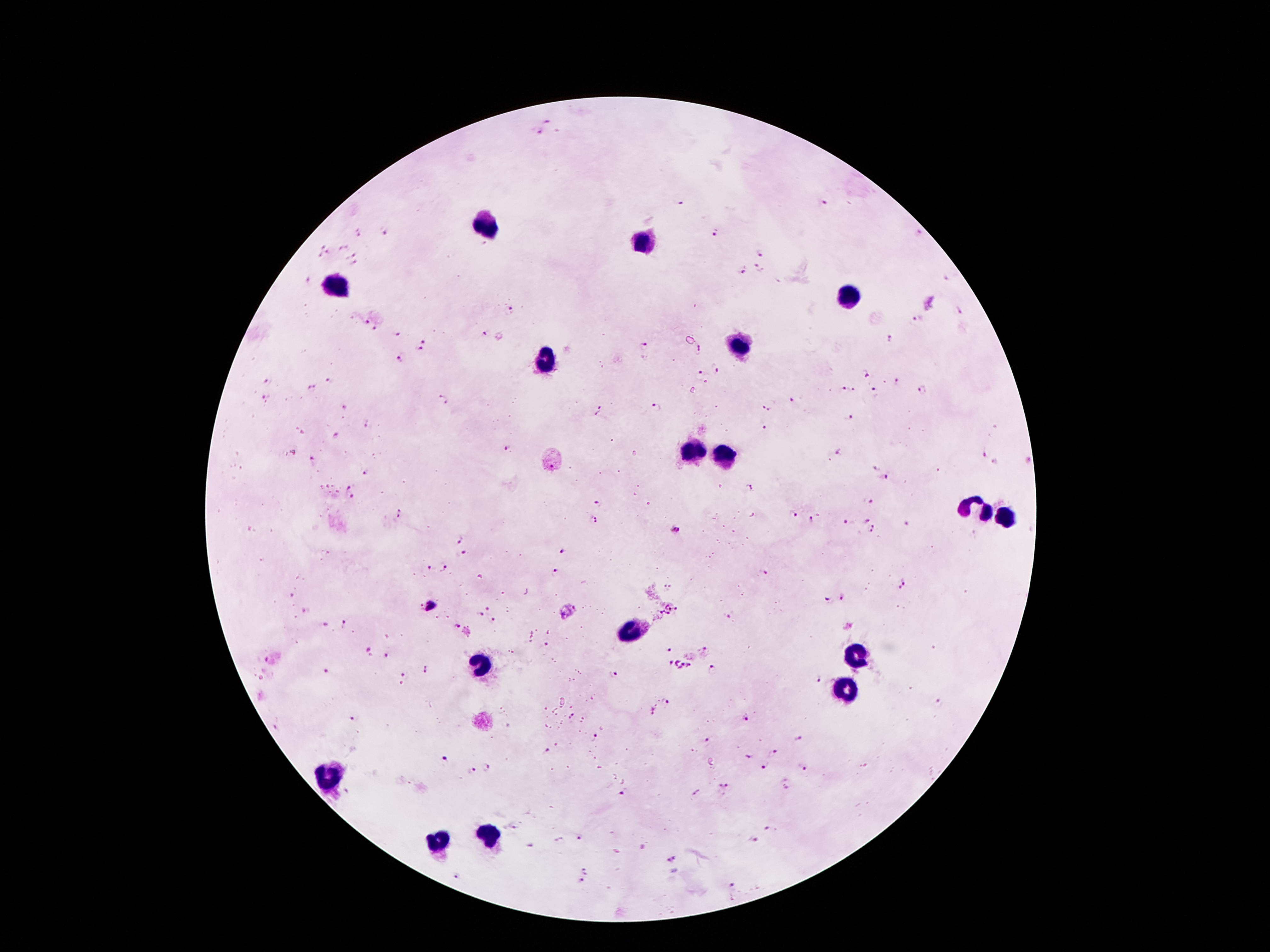

Approximate object centers, in pixels from the top-left corner.
Summary:
  - Plasmodium parasite locations: (x=548, y=121), (x=536, y=131), (x=680, y=202), (x=824, y=202), (x=358, y=231), (x=716, y=231), (x=383, y=233), (x=919, y=234), (x=323, y=244), (x=342, y=247), (x=330, y=252), (x=761, y=252), (x=351, y=254), (x=318, y=255), (x=354, y=262), (x=743, y=269), (x=760, y=269), (x=309, y=278), (x=945, y=279), (x=931, y=303), (x=511, y=310), (x=959, y=311), (x=918, y=320), (x=365, y=321), (x=374, y=328), (x=485, y=335), (x=398, y=336), (x=887, y=340), (x=423, y=341), (x=644, y=346), (x=420, y=348), (x=699, y=349), (x=399, y=360), (x=716, y=368), (x=700, y=374), (x=867, y=374), (x=328, y=381), (x=267, y=382), (x=897, y=383), (x=311, y=389), (x=854, y=390), (x=923, y=390), (x=844, y=391), (x=875, y=393), (x=267, y=398), (x=443, y=398), (x=791, y=400), (x=344, y=406), (x=601, y=406), (x=657, y=408), (x=767, y=408), (x=596, y=414), (x=849, y=416), (x=366, y=425), (x=763, y=428), (x=336, y=434), (x=840, y=449), (x=507, y=450), (x=984, y=453), (x=313, y=459), (x=1026, y=460), (x=995, y=461), (x=875, y=467), (x=366, y=470), (x=885, y=478), (x=350, y=487), (x=748, y=487), (x=352, y=495), (x=598, y=500), (x=868, y=500), (x=792, y=514), (x=400, y=515), (x=594, y=518), (x=866, y=518), (x=812, y=519), (x=847, y=522), (x=907, y=524), (x=872, y=529), (x=675, y=530), (x=460, y=538), (x=464, y=551), (x=562, y=552), (x=428, y=566), (x=442, y=566), (x=556, y=571), (x=763, y=572), (x=903, y=583), (x=668, y=587), (x=293, y=595), (x=843, y=596), (x=827, y=599), (x=431, y=606), (x=488, y=608), (x=669, y=610), (x=304, y=611), (x=479, y=614), (x=729, y=616), (x=495, y=620), (x=342, y=624), (x=325, y=626), (x=458, y=626), (x=548, y=646), (x=705, y=647), (x=670, y=648), (x=368, y=650), (x=386, y=656), (x=267, y=659), (x=681, y=665), (x=426, y=669), (x=713, y=671), (x=326, y=672), (x=614, y=673), (x=406, y=674), (x=817, y=678), (x=938, y=702), (x=666, y=703), (x=650, y=712), (x=571, y=717), (x=746, y=717), (x=354, y=718), (x=276, y=727), (x=596, y=735), (x=799, y=737), (x=705, y=740), (x=547, y=750), (x=774, y=752), (x=747, y=756), (x=446, y=760), (x=764, y=766), (x=486, y=768), (x=804, y=769), (x=471, y=771), (x=723, y=786), (x=624, y=792), (x=696, y=793), (x=514, y=828), (x=770, y=828), (x=580, y=839), (x=562, y=840), (x=755, y=840), (x=530, y=845), (x=672, y=859), (x=586, y=869), (x=457, y=876), (x=579, y=885), (x=733, y=885)
  - Leukocyte locations: (x=482, y=227), (x=646, y=242), (x=340, y=286), (x=850, y=295), (x=739, y=345), (x=545, y=360), (x=690, y=452), (x=724, y=458), (x=974, y=504), (x=1003, y=519), (x=634, y=626), (x=856, y=653), (x=480, y=662), (x=846, y=687), (x=329, y=777), (x=493, y=834), (x=438, y=842)
  - Stain: Giemsa
  - Preparation: thick peripheral-blood smear
  - Magnification: 100x
  - Image size: 1270×952 pixels
  - Capture: smartphone through the microscope eyepiece
  - Patient malaria status: infected with Plasmodium falciparum
  - Field of view: one from this slide